Assess this cell for malaria.
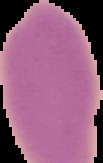

It is uninfected.

From a thin blood film. The area outside the segmented cell region is set to black. Image is 103×163 pixels.